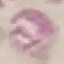

Malaria status: uninfected. Acquired by smartphone through the microscope eyepiece. Giemsa stain. Thin smear of blood. Cell patch, automatically extracted from a larger field of view and resized to 64 × 64 pixels.